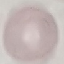 Malaria status: uninfected. Giemsa-stained preparation. Cell patch, automatically extracted from a larger field of view and resized to 64 × 64 pixels. Thin blood smear. Photographed with a smartphone camera at the microscope eyepiece.